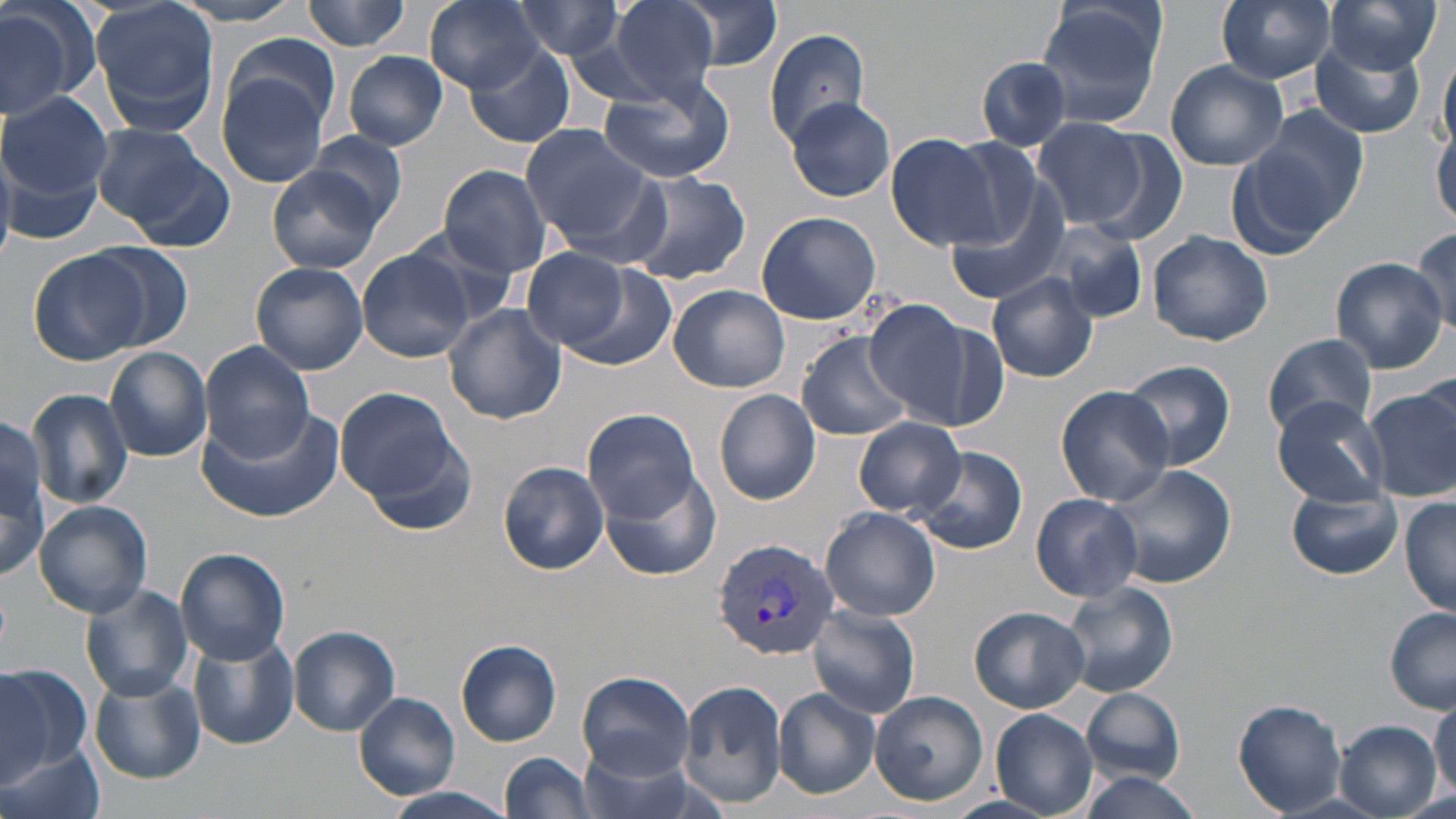

Approximate bounding boxes as [x1, y1, x2, y2] in pixels. Plasmodium vivax-infected red blood cell locations: [713, 539, 840, 658]. Uninfected red blood cell locations: [0, 0, 98, 122], [89, 0, 222, 135], [166, 0, 314, 27], [303, 0, 411, 51], [423, 0, 547, 93], [603, 0, 724, 99], [670, 0, 785, 73], [1217, 0, 1337, 83], [1325, 0, 1440, 74], [507, 1, 630, 61], [1034, 1, 1168, 129], [1191, 4, 1324, 151], [763, 29, 871, 140], [226, 33, 342, 133], [464, 39, 574, 148], [1309, 42, 1426, 139], [344, 50, 447, 149], [1438, 52, 1455, 154], [975, 56, 1077, 153], [1165, 62, 1287, 171], [218, 70, 334, 188], [597, 75, 734, 183], [2, 93, 113, 203], [784, 95, 896, 202], [1238, 110, 1367, 244], [1033, 117, 1149, 232], [519, 122, 653, 243], [92, 123, 229, 243], [1432, 124, 1456, 228], [1082, 129, 1194, 244], [304, 131, 409, 230], [885, 133, 999, 250], [438, 164, 552, 277], [266, 168, 384, 272], [618, 170, 750, 286], [944, 172, 1073, 306], [757, 210, 881, 325], [1048, 222, 1150, 323], [402, 224, 525, 321], [1408, 227, 1455, 334], [1148, 230, 1274, 346], [87, 242, 195, 351], [27, 248, 152, 367], [357, 248, 474, 363], [519, 249, 634, 350], [1330, 258, 1449, 373], [548, 261, 681, 374], [250, 262, 368, 374], [987, 273, 1099, 383], [669, 285, 790, 394], [863, 298, 985, 428], [443, 303, 567, 424], [796, 331, 915, 441], [1261, 333, 1380, 439], [198, 339, 315, 462], [104, 347, 212, 462], [1120, 359, 1235, 471], [335, 386, 467, 512], [1364, 386, 1455, 501], [26, 387, 135, 512], [1057, 387, 1174, 504], [715, 389, 821, 506], [1272, 397, 1390, 505], [193, 405, 344, 524], [584, 409, 702, 525], [0, 416, 50, 580], [855, 418, 965, 517], [356, 428, 477, 539], [911, 444, 1028, 555], [497, 461, 610, 574], [1103, 463, 1237, 590], [598, 468, 722, 580], [1288, 485, 1404, 580], [1031, 493, 1143, 601], [1400, 496, 1456, 616], [35, 500, 152, 616], [820, 507, 941, 620], [175, 547, 291, 663], [1061, 581, 1178, 698], [79, 583, 193, 701], [807, 605, 921, 718], [969, 605, 1090, 712], [1385, 607, 1456, 713], [290, 625, 400, 736], [187, 633, 297, 750], [456, 639, 562, 746], [0, 662, 89, 783], [578, 670, 695, 779], [89, 675, 205, 783], [679, 678, 789, 810], [1081, 688, 1185, 784], [773, 689, 881, 800], [870, 690, 988, 806], [354, 693, 460, 798], [1429, 695, 1456, 802], [1233, 699, 1348, 814], [990, 708, 1100, 816], [1333, 721, 1441, 816], [574, 738, 711, 819], [0, 742, 106, 819], [500, 752, 597, 818], [1074, 770, 1206, 819], [382, 787, 518, 818]. Slide-level diagnosis: Plasmodium vivax. Single field of view. May-Grünwald-Giemsa-stained preparation. Optical microscopy. Image is 1456×819 pixels. Thin blood smear. Captured at 1000x magnification.